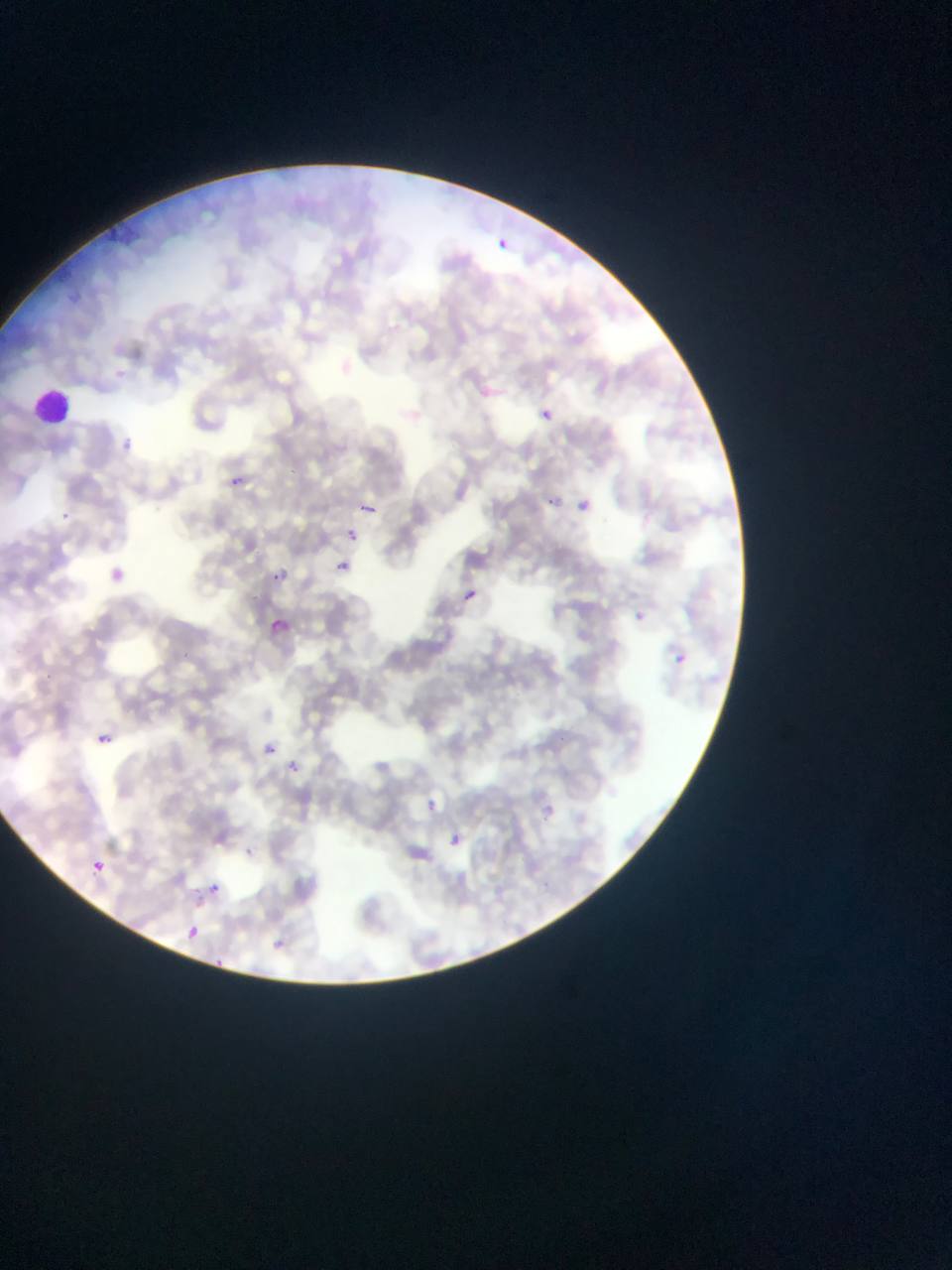

Approximate bounding boxes as left top right bottom in pixels.
Summary:
  - Plasmodium parasite locations: 496 238 508 249; 475 383 495 401; 539 409 552 421; 224 473 245 492; 544 494 560 510; 576 497 592 513; 360 500 380 517; 346 517 367 542; 344 527 362 544; 333 558 351 576; 101 562 130 588; 269 567 289 587; 463 588 478 602; 266 615 293 640; 673 652 688 667; 96 733 112 747; 256 737 281 761; 281 755 307 780; 417 794 444 820; 538 804 558 823; 441 827 468 854; 89 858 107 875; 206 881 222 896; 183 924 204 944; 266 934 292 957; 211 956 226 970
  - Field of view: single
  - Preparation: thin blood smear
  - Image size: 952×1270 pixels
  - Country: Ghana
  - Capture: mobile-phone photograph through a microscope